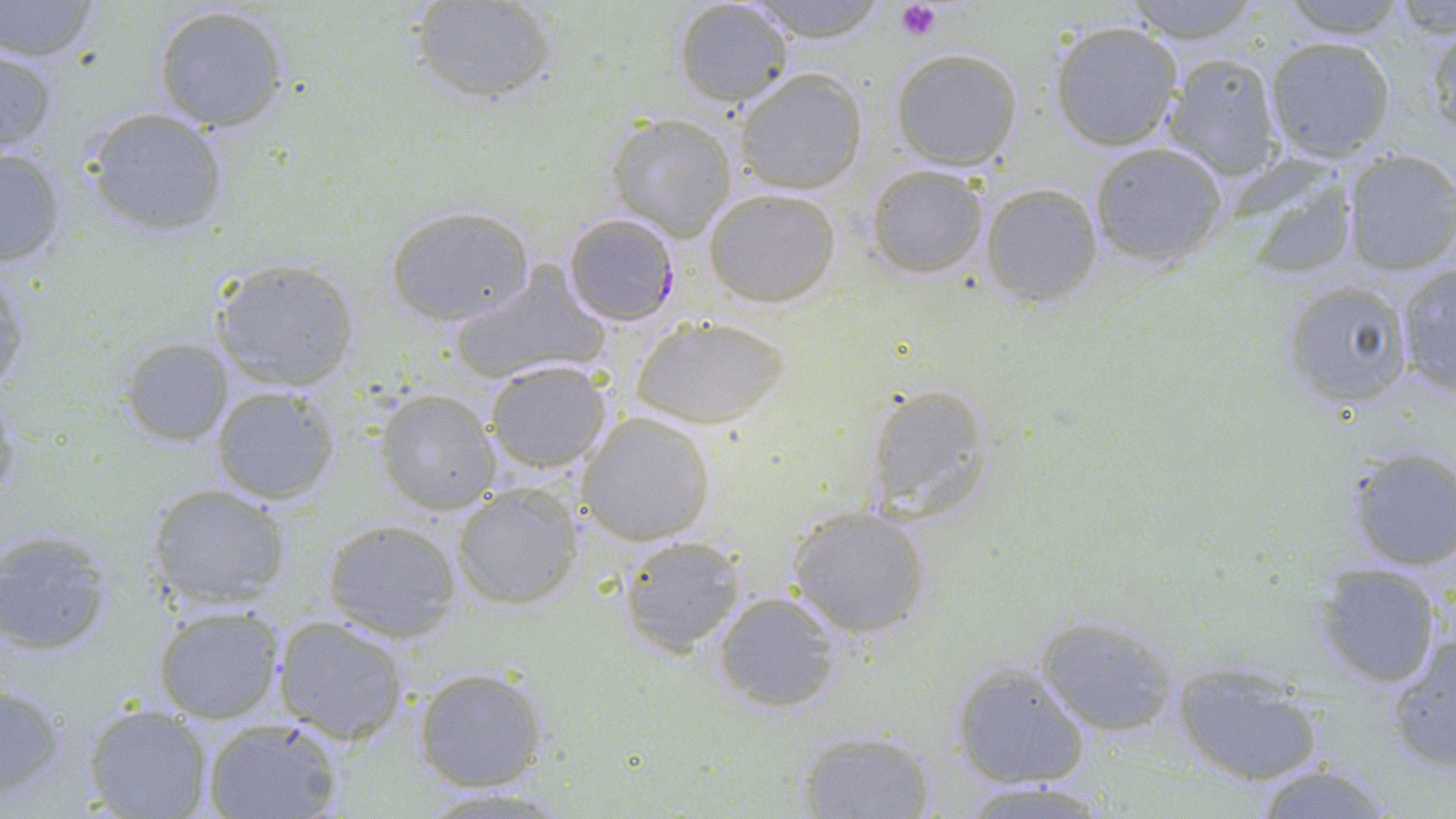

slide-level diagnosis = Plasmodium falciparum
preparation = thin blood smear
Plasmodium falciparum-infected red blood cell locations = approximate bounding boxes as (x1,y1)-(x2,y2) corner pairs in pixels: (561,213)-(683,328)
magnification = 1000x
uninfected red blood cell locations = approximate bounding boxes as (x1,y1)-(x2,y2) corner pairs in pixels: (1,0)-(104,62), (413,0)-(559,107), (671,0)-(796,110), (748,0)-(887,43), (1272,0)-(1413,38), (1123,2)-(1264,43), (1385,3)-(1456,37), (151,4)-(293,134), (1051,21)-(1184,152), (1426,21)-(1456,139), (1265,37)-(1397,162), (0,43)-(60,157), (891,48)-(1024,170), (1163,52)-(1284,181), (735,69)-(868,195), (84,107)-(230,236), (607,113)-(737,239), (1088,142)-(1227,266), (0,144)-(70,270), (1341,149)-(1456,277), (1235,163)-(1361,278), (865,164)-(989,278), (980,183)-(1103,306), (703,188)-(843,309), (383,204)-(536,326), (211,257)-(362,393), (0,258)-(31,400), (1394,264)-(1455,395), (447,265)-(612,386), (1279,280)-(1415,412), (629,315)-(793,430), (120,337)-(233,447), (484,359)-(613,474), (862,382)-(997,525), (209,385)-(343,505), (374,389)-(501,515), (576,411)-(716,545), (1344,447)-(1456,573), (146,481)-(294,610), (451,482)-(585,610), (787,506)-(933,639), (322,518)-(461,642), (0,529)-(116,655), (617,534)-(746,655), (1311,561)-(1443,688), (713,590)-(844,713), (152,603)-(285,725), (1036,612)-(1183,738), (274,615)-(410,744), (1382,632)-(1456,773), (950,659)-(1091,790), (1172,663)-(1322,785), (413,665)-(550,792), (0,683)-(67,803), (82,703)-(212,819), (199,718)-(343,819), (793,729)-(937,818), (1248,761)-(1397,819), (955,778)-(1118,817), (410,785)-(581,816)
field of view = single
modality = light microscopy
image size = 1456×819 pixels
platelet locations = approximate bounding boxes as (x1,y1)-(x2,y2) corner pairs in pixels: (895,1)-(941,41)
stain = May-Grünwald-Giemsa